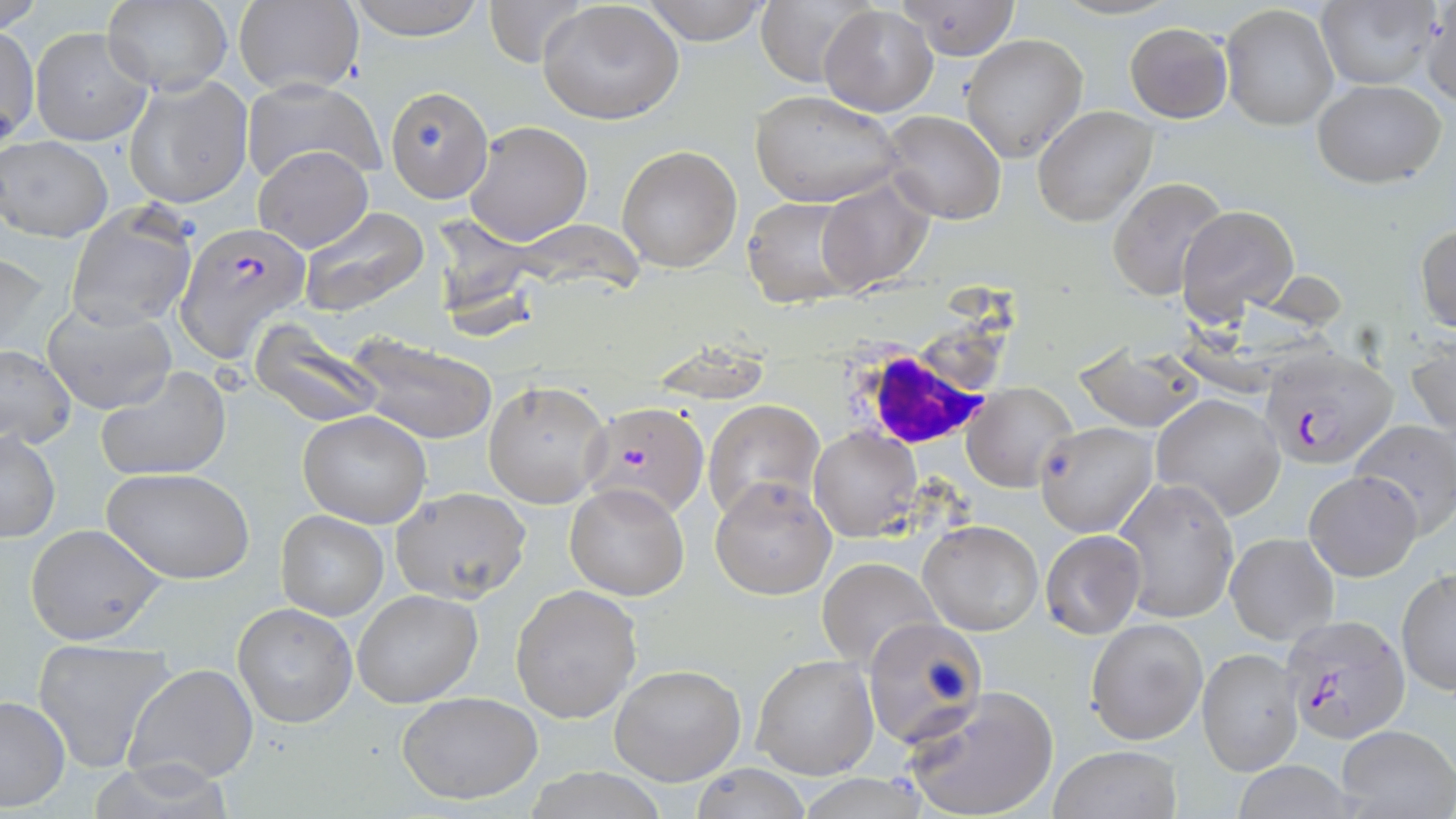
Summary:
  - Coordinate format: approximate bounding boxes as named x1/y1/x2/y2 corners in pixels
  - White blood cell locations: (x1=847, y1=340, x2=999, y2=454)
  - Uninfected red blood cell locations: (x1=1, y1=0, x2=44, y2=32), (x1=342, y1=0, x2=490, y2=40), (x1=483, y1=0, x2=588, y2=70), (x1=639, y1=0, x2=771, y2=45), (x1=896, y1=0, x2=1023, y2=60), (x1=757, y1=1, x2=875, y2=88), (x1=1316, y1=1, x2=1439, y2=90), (x1=1421, y1=1, x2=1456, y2=110), (x1=101, y1=2, x2=231, y2=94), (x1=231, y1=2, x2=366, y2=96), (x1=537, y1=2, x2=683, y2=125), (x1=1220, y1=4, x2=1338, y2=132), (x1=819, y1=5, x2=937, y2=117), (x1=1125, y1=22, x2=1233, y2=122), (x1=0, y1=26, x2=39, y2=146), (x1=29, y1=26, x2=152, y2=145), (x1=961, y1=33, x2=1088, y2=162), (x1=125, y1=74, x2=252, y2=209), (x1=242, y1=78, x2=385, y2=189), (x1=1311, y1=80, x2=1446, y2=188), (x1=384, y1=86, x2=494, y2=203), (x1=748, y1=90, x2=904, y2=207), (x1=1032, y1=105, x2=1158, y2=228), (x1=878, y1=111, x2=1006, y2=225), (x1=465, y1=120, x2=593, y2=244), (x1=1, y1=136, x2=113, y2=241), (x1=251, y1=145, x2=373, y2=253), (x1=616, y1=145, x2=742, y2=273), (x1=814, y1=177, x2=935, y2=296), (x1=1107, y1=177, x2=1230, y2=301), (x1=743, y1=195, x2=863, y2=309), (x1=66, y1=203, x2=198, y2=332), (x1=1174, y1=203, x2=1300, y2=329), (x1=297, y1=206, x2=431, y2=317), (x1=429, y1=214, x2=547, y2=334), (x1=1416, y1=224, x2=1456, y2=332), (x1=1, y1=250, x2=51, y2=362), (x1=43, y1=300, x2=177, y2=415), (x1=250, y1=321, x2=386, y2=430), (x1=349, y1=333, x2=496, y2=447), (x1=1407, y1=336, x2=1456, y2=444), (x1=1075, y1=344, x2=1205, y2=433), (x1=0, y1=345, x2=75, y2=449), (x1=97, y1=366, x2=231, y2=483), (x1=484, y1=381, x2=610, y2=507), (x1=962, y1=383, x2=1078, y2=494), (x1=1152, y1=394, x2=1285, y2=520), (x1=702, y1=398, x2=826, y2=522), (x1=299, y1=411, x2=433, y2=528), (x1=1348, y1=418, x2=1456, y2=534), (x1=1034, y1=421, x2=1157, y2=537), (x1=809, y1=428, x2=920, y2=540), (x1=1, y1=431, x2=60, y2=541), (x1=103, y1=466, x2=256, y2=583), (x1=1306, y1=470, x2=1421, y2=581), (x1=709, y1=477, x2=837, y2=602), (x1=1114, y1=478, x2=1238, y2=623), (x1=564, y1=483, x2=689, y2=600), (x1=388, y1=489, x2=532, y2=605), (x1=275, y1=510, x2=388, y2=621), (x1=918, y1=519, x2=1043, y2=636), (x1=24, y1=524, x2=168, y2=645), (x1=1039, y1=530, x2=1148, y2=641), (x1=1226, y1=533, x2=1338, y2=644), (x1=816, y1=557, x2=941, y2=670), (x1=1397, y1=569, x2=1456, y2=693), (x1=510, y1=585, x2=642, y2=724), (x1=352, y1=589, x2=483, y2=708), (x1=234, y1=603, x2=357, y2=728), (x1=862, y1=617, x2=988, y2=749), (x1=1086, y1=618, x2=1208, y2=746), (x1=32, y1=637, x2=176, y2=773), (x1=1197, y1=647, x2=1303, y2=776), (x1=751, y1=655, x2=879, y2=781), (x1=124, y1=663, x2=258, y2=785), (x1=608, y1=664, x2=748, y2=786), (x1=900, y1=684, x2=1061, y2=819), (x1=396, y1=692, x2=544, y2=805), (x1=0, y1=695, x2=71, y2=811), (x1=1337, y1=724, x2=1455, y2=817), (x1=1049, y1=745, x2=1182, y2=819), (x1=1228, y1=761, x2=1365, y2=819), (x1=686, y1=763, x2=813, y2=819), (x1=525, y1=769, x2=668, y2=819), (x1=795, y1=775, x2=934, y2=817)
  - Plasmodium falciparum-infected red blood cell locations: (x1=175, y1=223, x2=308, y2=362), (x1=1261, y1=345, x2=1399, y2=471), (x1=572, y1=400, x2=713, y2=533), (x1=1280, y1=613, x2=1410, y2=743)
  - Slide-level diagnosis: Plasmodium falciparum
  - Stain: May-Grünwald-Giemsa
  - Field of view: one of a larger specimen
  - Magnification: 1000x
  - Image size: 1456×819 pixels
  - Modality: light microscopy
  - Preparation: thin blood film